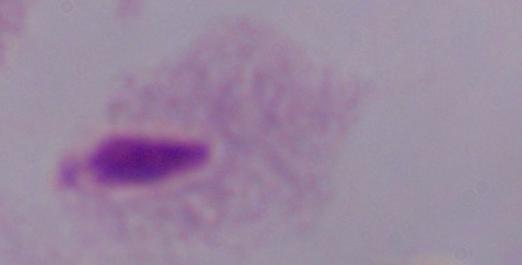

Summary:
  - Magnification: 1000x
  - Identification: trichomonad
  - Modality: photomicrograph